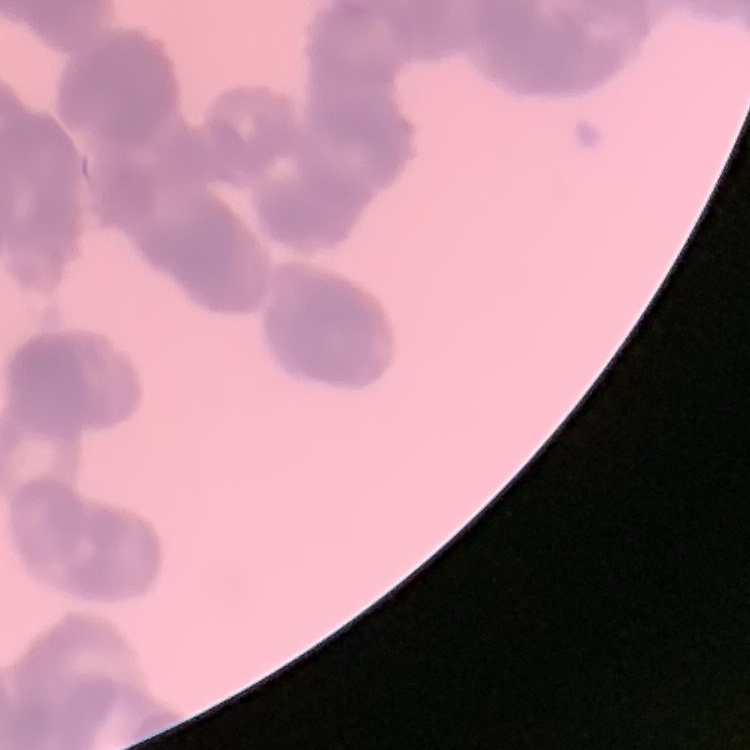

{
  "erythrocyte_morphology": "rouleaux formation",
  "image_type": "one tile cut from a larger photomicrograph",
  "stain": "Field's or Giemsa",
  "preparation": "thin blood smear"
}